Assess the morphology of the red blood cells.
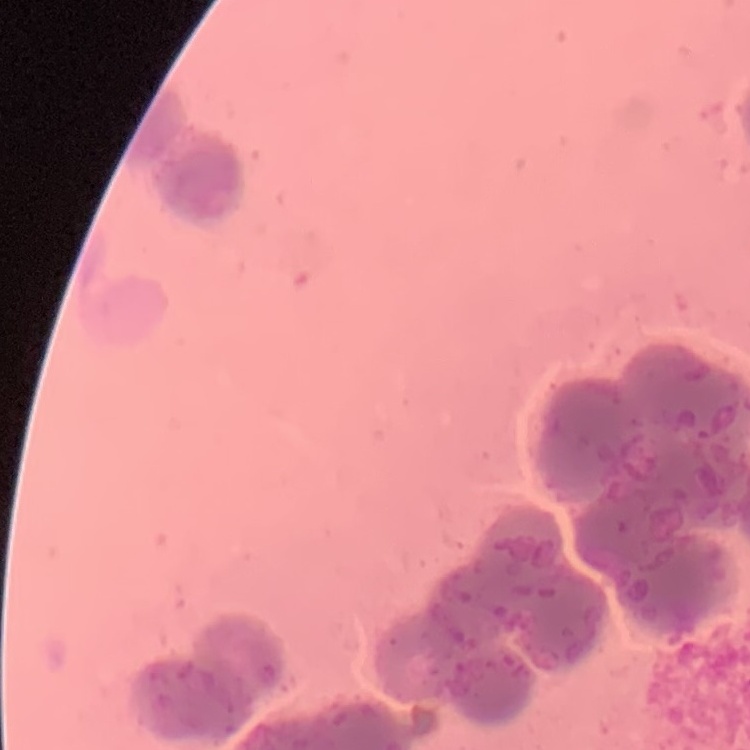

They show rouleaux formation.

Square crop of a larger photomicrograph. Stained with either Field's or Giemsa. Thin peripheral smear.